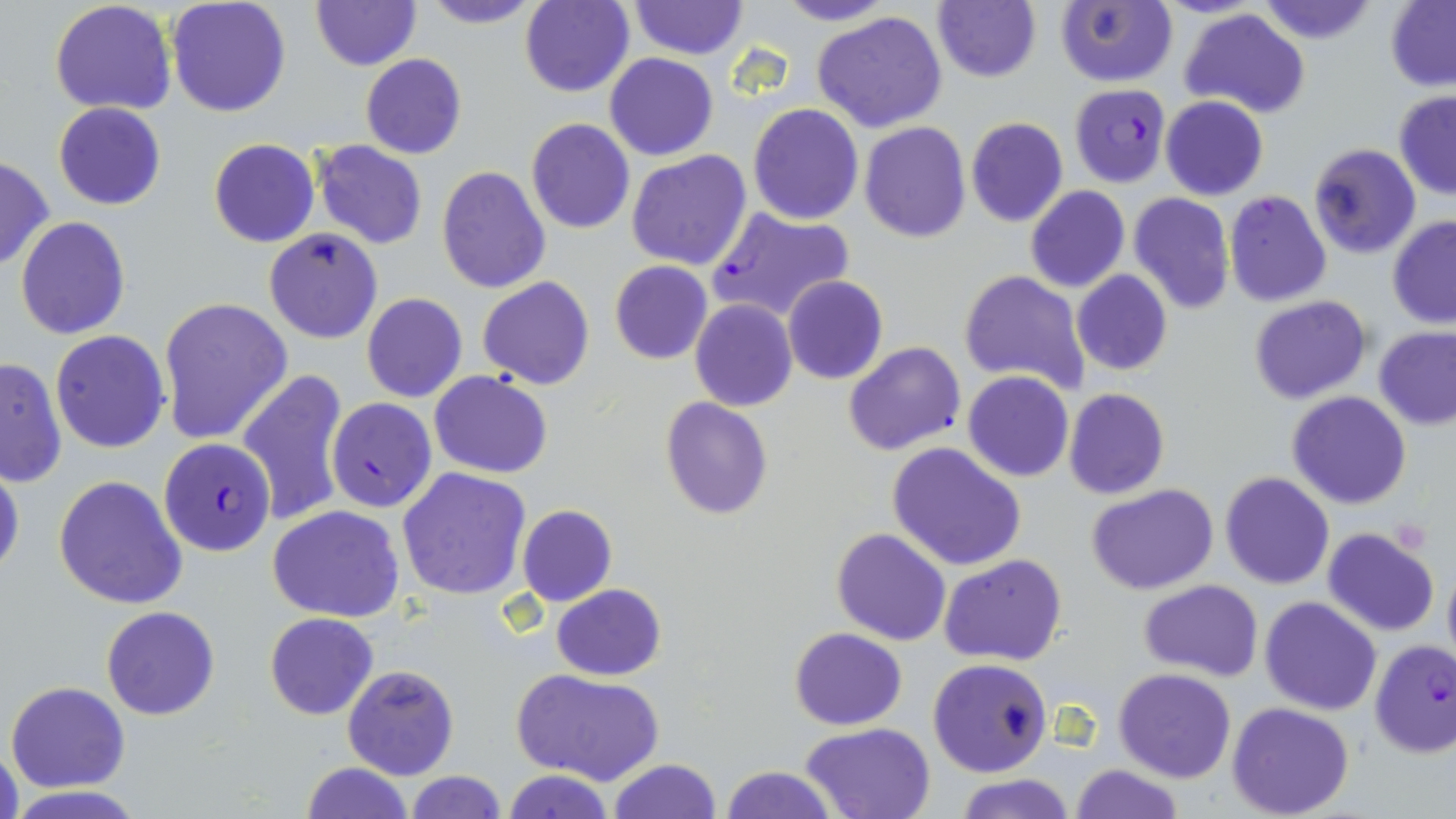
Approximate bounding boxes as (x1, y1, x2, y2) in pixels. Plasmodium falciparum-infected red blood cell locations: (1070, 85, 1170, 188), (706, 203, 857, 320), (328, 398, 436, 513), (158, 436, 277, 559). Uninfected red blood cell locations: (167, 0, 291, 118), (311, 0, 419, 71), (415, 0, 548, 29), (772, 0, 899, 27), (933, 0, 1042, 84), (1254, 0, 1381, 47), (519, 1, 635, 97), (627, 1, 748, 59), (1054, 1, 1178, 87), (50, 2, 176, 116), (1385, 2, 1456, 89), (1180, 8, 1311, 119), (811, 10, 950, 134), (606, 52, 718, 160), (360, 53, 467, 158), (1393, 92, 1456, 200), (1161, 96, 1268, 201), (53, 101, 166, 210), (748, 102, 863, 224), (965, 116, 1068, 227), (525, 117, 635, 234), (859, 122, 972, 243), (470, 124, 609, 258), (208, 139, 320, 248), (314, 141, 429, 251), (1309, 144, 1421, 260), (626, 150, 752, 272), (0, 156, 53, 272), (437, 165, 550, 293), (1025, 186, 1130, 294), (1224, 191, 1331, 308), (1127, 192, 1235, 315), (14, 216, 131, 339), (1387, 216, 1456, 328), (263, 227, 384, 345), (609, 260, 713, 365), (958, 269, 1090, 394), (1072, 270, 1173, 376), (478, 276, 594, 390), (783, 276, 889, 385), (361, 293, 467, 403), (1249, 296, 1371, 405), (157, 297, 293, 444), (690, 299, 798, 412), (1373, 326, 1456, 429), (49, 330, 171, 453), (843, 341, 966, 456), (0, 357, 67, 488), (238, 368, 349, 528), (430, 370, 552, 479), (963, 371, 1075, 482), (1063, 388, 1169, 500), (1287, 392, 1413, 510), (660, 396, 773, 518), (888, 442, 1025, 572), (0, 459, 24, 584), (397, 467, 531, 599), (1220, 472, 1334, 589), (53, 476, 187, 610), (1086, 484, 1219, 596), (517, 504, 617, 606), (267, 506, 405, 622), (831, 527, 953, 646), (1323, 527, 1439, 637), (1442, 552, 1456, 670), (939, 554, 1067, 667), (1139, 581, 1261, 681), (552, 584, 667, 680), (1259, 596, 1382, 715), (101, 606, 220, 720), (265, 612, 379, 720), (789, 628, 907, 729), (1368, 640, 1456, 758), (927, 657, 1053, 776), (343, 665, 459, 780), (1114, 667, 1236, 782), (514, 670, 663, 787), (7, 681, 130, 792), (1227, 702, 1355, 819), (800, 722, 936, 817), (0, 744, 23, 819), (608, 758, 723, 818), (300, 761, 414, 818), (1070, 764, 1183, 819), (719, 765, 837, 819), (502, 770, 617, 819), (403, 772, 507, 818), (957, 773, 1074, 819), (10, 788, 151, 817). Slide-level diagnosis: Plasmodium falciparum. May-Grünwald-Giemsa-stained preparation. Image is 1456×819 pixels. Single field of view. Thin blood smear. Optical microscopy. Captured at 1000x magnification.